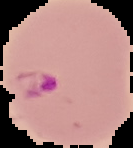

Summary:
  - Image type: segmented cell region on a black background
  - Image size: 133×148 pixels
  - Preparation: thin blood film
  - Malaria status: parasitized